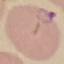

Malaria status: parasitized. Acquired by smartphone through the microscope eyepiece. Cell patch, automatically extracted from a larger field of view and resized to 64 × 64 pixels. Giemsa stain. Thin blood film.